Classify this cell by malaria status.
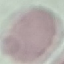

Uninfected.

Thin blood smear. Acquired by smartphone through the microscope eyepiece. Giemsa stain. Cell patch, automatically extracted from a larger field of view and resized to 64 × 64 pixels.